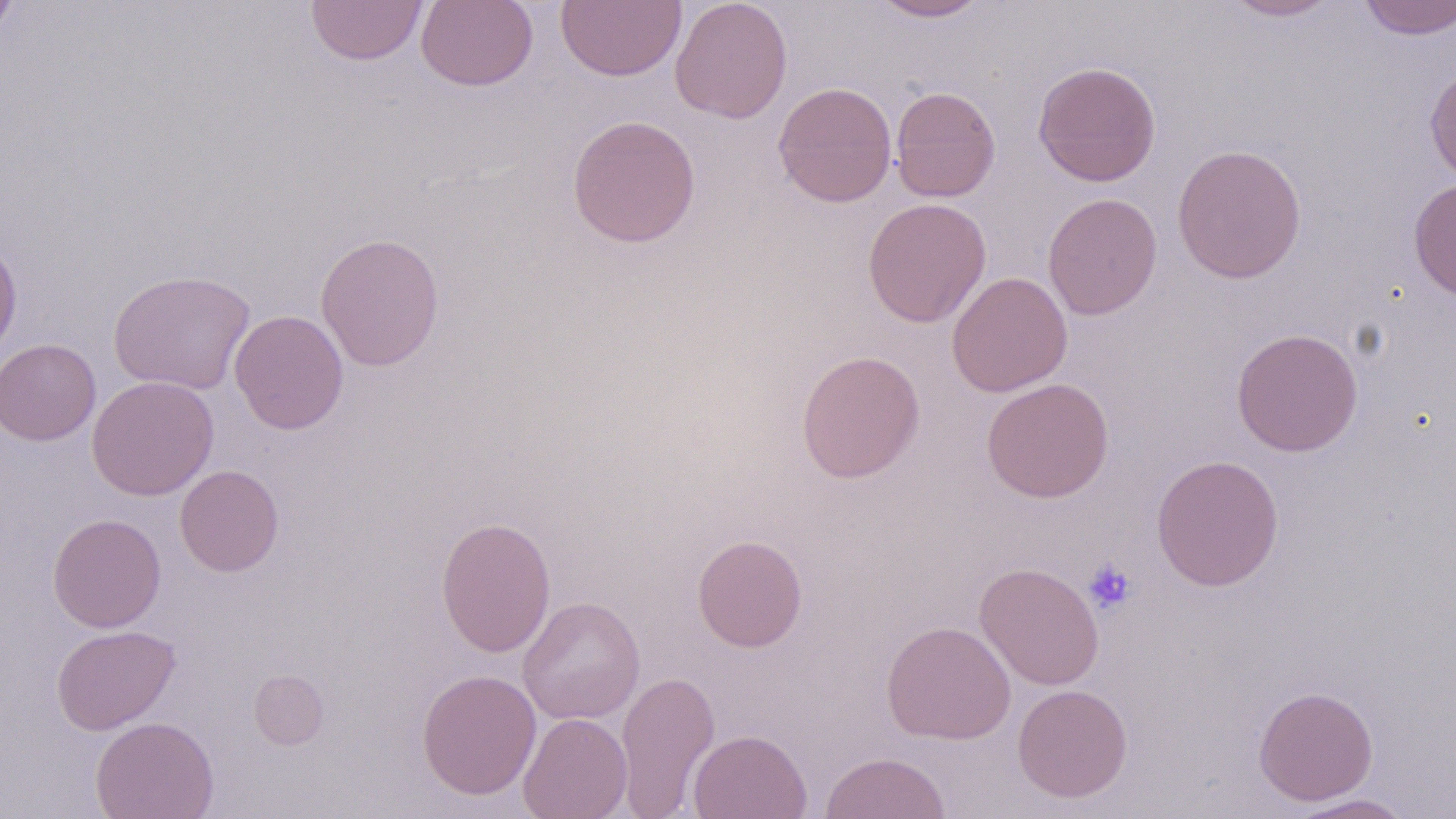

Summary:
  - Coordinate format: approximate bounding boxes as (x1, y1, x2, y2) in pixels
  - Uninfected red blood cell locations: (0, 0, 18, 45), (304, 0, 428, 65), (415, 0, 539, 91), (557, 0, 686, 82), (670, 0, 793, 123), (871, 0, 992, 22), (1220, 0, 1341, 21), (1358, 0, 1456, 40), (1033, 61, 1162, 187), (1424, 62, 1456, 185), (773, 81, 897, 207), (889, 85, 1001, 202), (567, 114, 701, 248), (1172, 143, 1307, 284), (1407, 178, 1456, 302), (1042, 193, 1162, 320), (862, 197, 991, 328), (315, 232, 444, 372), (0, 237, 22, 360), (108, 269, 256, 395), (946, 271, 1073, 397), (229, 310, 349, 434), (1231, 327, 1363, 457), (0, 339, 101, 445), (795, 349, 926, 484), (87, 375, 219, 501), (981, 377, 1114, 502), (1151, 454, 1285, 591), (174, 464, 284, 577), (47, 513, 166, 633), (436, 515, 556, 657), (692, 534, 808, 652), (974, 562, 1105, 690), (517, 596, 645, 725), (881, 620, 1016, 745), (51, 624, 180, 735), (248, 669, 329, 749), (416, 669, 542, 800), (615, 669, 720, 818), (1013, 684, 1133, 802), (1253, 685, 1378, 805), (518, 712, 632, 818), (90, 715, 219, 819), (688, 729, 812, 819), (820, 751, 951, 819), (1285, 793, 1417, 818)
  - Platelet locations: (1083, 559, 1137, 614)
  - Slide-level diagnosis: no evidence of blood parasites
  - Preparation: thin blood smear
  - Stain: May-Grünwald-Giemsa
  - Field of view: single
  - Modality: light microscopy
  - Magnification: 1000x
  - Image size: 1456×819 pixels